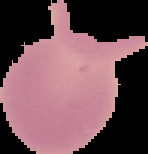
image size = 148×154 pixels
malaria status = uninfected
image type = segmented cell region on a black background
preparation = thin blood smear